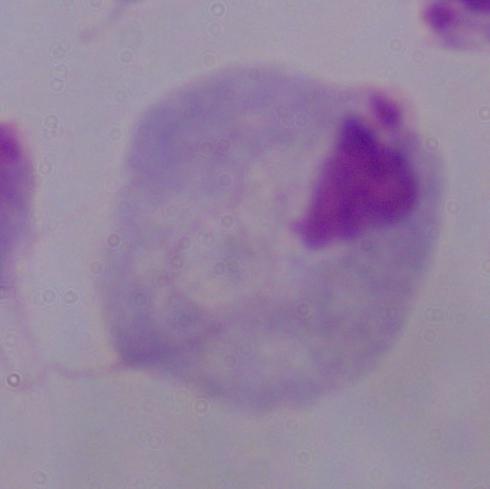

A trichomonad is shown. Photomicrograph. 1000x magnification.